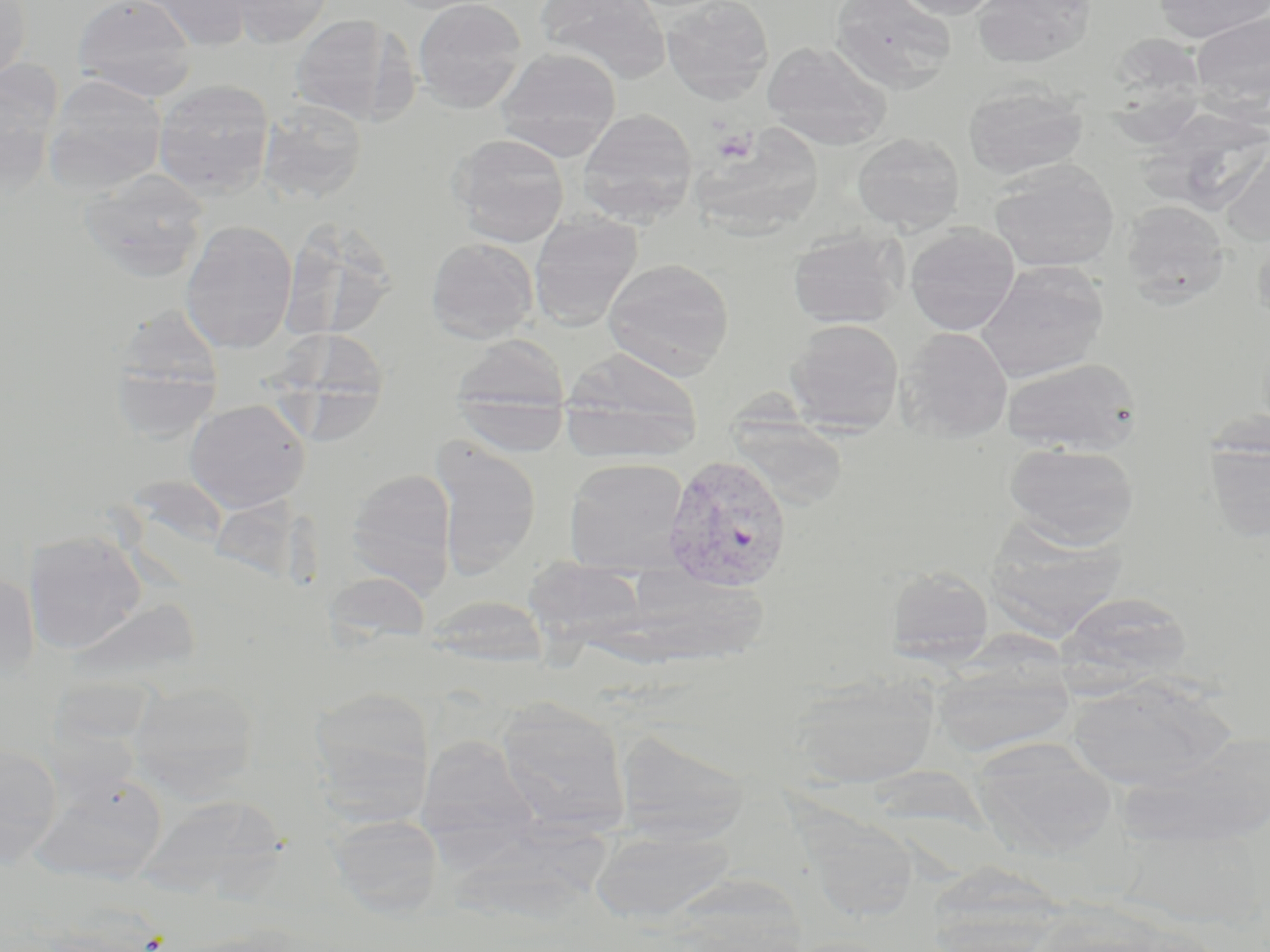

Summary:
  - Coordinate format: approximate bounding boxes as named x1/y1/x2/y2 corners in pixels
  - Uninfected red blood cell locations: (x1=0, y1=0, x2=32, y2=82), (x1=73, y1=0, x2=198, y2=101), (x1=134, y1=0, x2=254, y2=51), (x1=231, y1=0, x2=333, y2=48), (x1=412, y1=0, x2=527, y2=113), (x1=535, y1=0, x2=672, y2=84), (x1=661, y1=0, x2=774, y2=102), (x1=829, y1=0, x2=957, y2=92), (x1=892, y1=0, x2=1003, y2=20), (x1=971, y1=0, x2=1094, y2=68), (x1=1152, y1=1, x2=1270, y2=43), (x1=1190, y1=10, x2=1270, y2=114), (x1=290, y1=13, x2=414, y2=127), (x1=1117, y1=32, x2=1206, y2=157), (x1=762, y1=40, x2=891, y2=149), (x1=495, y1=47, x2=622, y2=160), (x1=1, y1=61, x2=62, y2=196), (x1=43, y1=75, x2=167, y2=195), (x1=153, y1=79, x2=275, y2=199), (x1=963, y1=82, x2=1089, y2=181), (x1=257, y1=100, x2=368, y2=206), (x1=577, y1=108, x2=698, y2=224), (x1=852, y1=132, x2=965, y2=234), (x1=449, y1=133, x2=570, y2=247), (x1=1220, y1=140, x2=1270, y2=244), (x1=989, y1=162, x2=1119, y2=273), (x1=79, y1=168, x2=210, y2=282), (x1=1121, y1=200, x2=1230, y2=301), (x1=286, y1=206, x2=401, y2=347), (x1=529, y1=213, x2=642, y2=330), (x1=180, y1=219, x2=298, y2=354), (x1=904, y1=224, x2=1020, y2=335), (x1=787, y1=228, x2=905, y2=328), (x1=1251, y1=230, x2=1270, y2=332), (x1=426, y1=237, x2=538, y2=343), (x1=603, y1=258, x2=734, y2=379), (x1=975, y1=261, x2=1108, y2=383), (x1=783, y1=316, x2=902, y2=430), (x1=896, y1=327, x2=1014, y2=442), (x1=268, y1=332, x2=397, y2=444), (x1=451, y1=334, x2=569, y2=418), (x1=108, y1=336, x2=223, y2=445), (x1=560, y1=348, x2=702, y2=461), (x1=1001, y1=356, x2=1142, y2=455), (x1=730, y1=389, x2=855, y2=486), (x1=456, y1=395, x2=569, y2=457), (x1=184, y1=398, x2=312, y2=512), (x1=429, y1=437, x2=542, y2=577), (x1=1205, y1=439, x2=1270, y2=542), (x1=1004, y1=442, x2=1139, y2=548), (x1=563, y1=457, x2=690, y2=574), (x1=346, y1=469, x2=457, y2=593), (x1=991, y1=522, x2=1131, y2=645), (x1=23, y1=531, x2=147, y2=654), (x1=530, y1=557, x2=655, y2=663), (x1=886, y1=565, x2=994, y2=664), (x1=0, y1=569, x2=39, y2=684), (x1=322, y1=570, x2=432, y2=649), (x1=1056, y1=591, x2=1192, y2=693), (x1=424, y1=594, x2=550, y2=668), (x1=932, y1=654, x2=1075, y2=758), (x1=790, y1=674, x2=938, y2=787), (x1=1068, y1=675, x2=1231, y2=790), (x1=127, y1=679, x2=262, y2=797), (x1=309, y1=687, x2=436, y2=819), (x1=496, y1=696, x2=629, y2=833), (x1=615, y1=728, x2=749, y2=844), (x1=1125, y1=731, x2=1270, y2=848), (x1=415, y1=734, x2=538, y2=855), (x1=971, y1=738, x2=1117, y2=857), (x1=0, y1=742, x2=62, y2=866), (x1=30, y1=775, x2=166, y2=884), (x1=137, y1=792, x2=290, y2=902), (x1=330, y1=814, x2=444, y2=918), (x1=457, y1=815, x2=616, y2=920), (x1=591, y1=825, x2=735, y2=923)
  - Plasmodium vivax-infected red blood cell locations: (x1=661, y1=456, x2=793, y2=596)
  - Platelet locations: (x1=710, y1=127, x2=757, y2=164)
  - Slide-level diagnosis: Plasmodium vivax
  - Magnification: 1000x
  - Stain: May-Grünwald-Giemsa
  - Modality: light microscopy
  - Field of view: one of a larger specimen
  - Image size: 1270×952 pixels
  - Preparation: thin blood smear